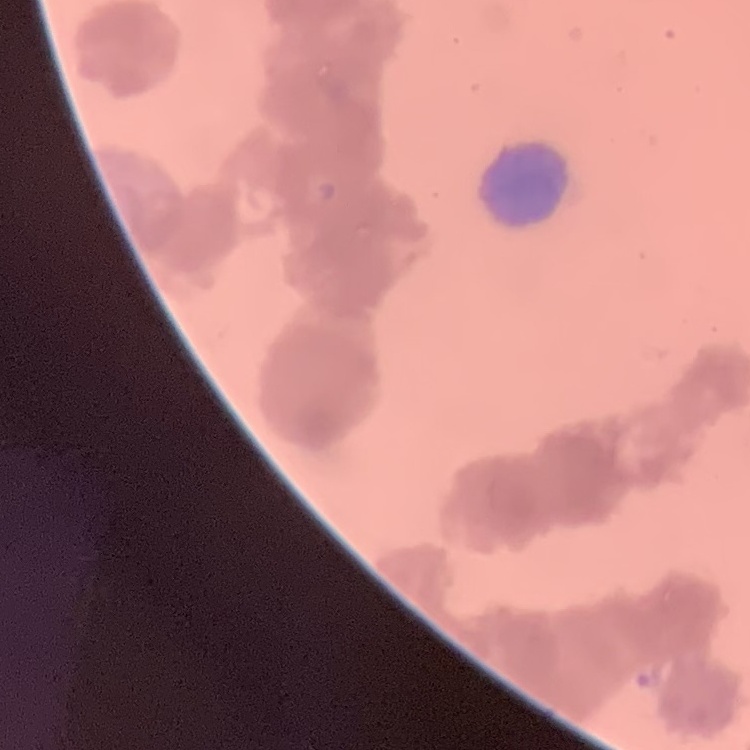 The red blood cells exhibit rouleaux formation. Stained with either Field's or Giemsa. Thin blood film. Square crop of a larger photomicrograph.